Comment on the morphology of the erythrocytes.
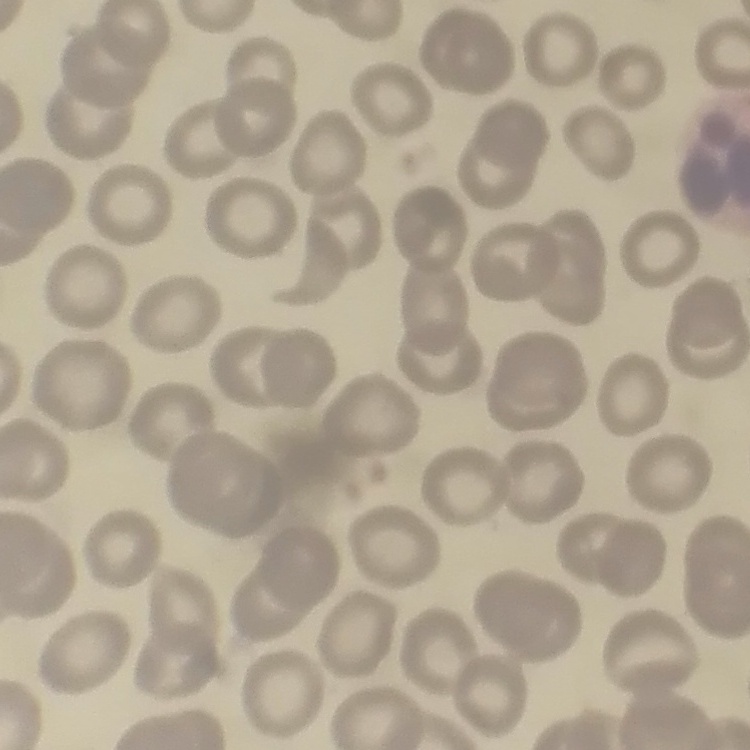

They show no rouleaux formation.

stain: Field's or Giemsa
image_type: one tile cut from a larger photomicrograph
preparation: thin blood smear